Report the malaria status of this cell.
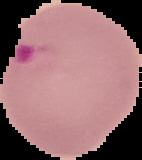
Parasitized.

image size = 142×160 pixels
preparation = thin blood smear
image type = segmented cell region on a black background